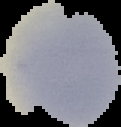
{
  "preparation": "thin blood smear",
  "image_type": "segmented cell region on a black background",
  "image_size": "121×127 pixels",
  "malaria_status": "uninfected"
}